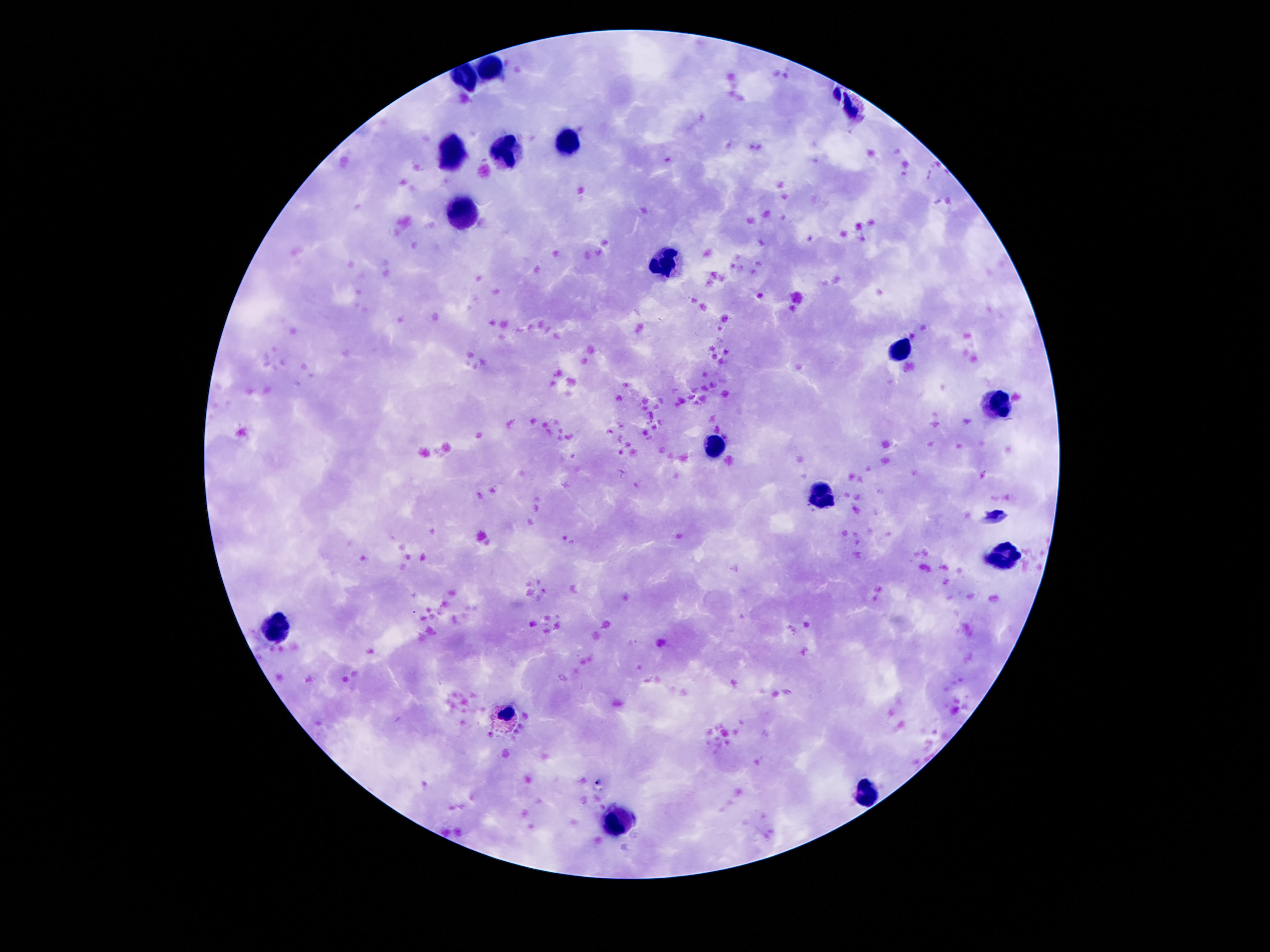
Approximate centers as (x, y) in pixels.
Summary:
  - Leukocyte locations: (488, 71), (467, 79), (567, 142), (452, 151), (506, 151), (463, 213), (668, 266), (899, 350), (995, 402), (714, 444), (821, 495), (1002, 554), (271, 627), (867, 791), (620, 822)
  - Capture: smartphone camera through the microscope eyepiece
  - Field of view: one from this slide
  - Stain: Giemsa
  - Image size: 1270×952 pixels
  - Preparation: thick peripheral-blood smear
  - Magnification: 100x
  - Patient malaria status: not infected